Identify the parasite.
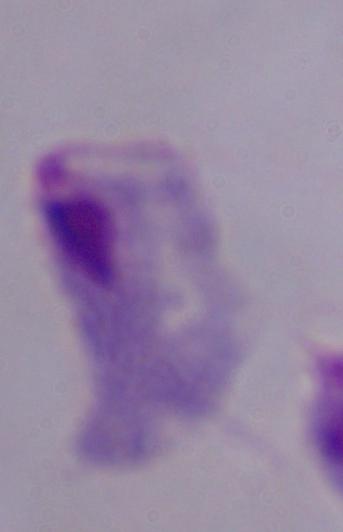
A trichomonad.

Summary:
  - Magnification: 1000x
  - Modality: micrograph